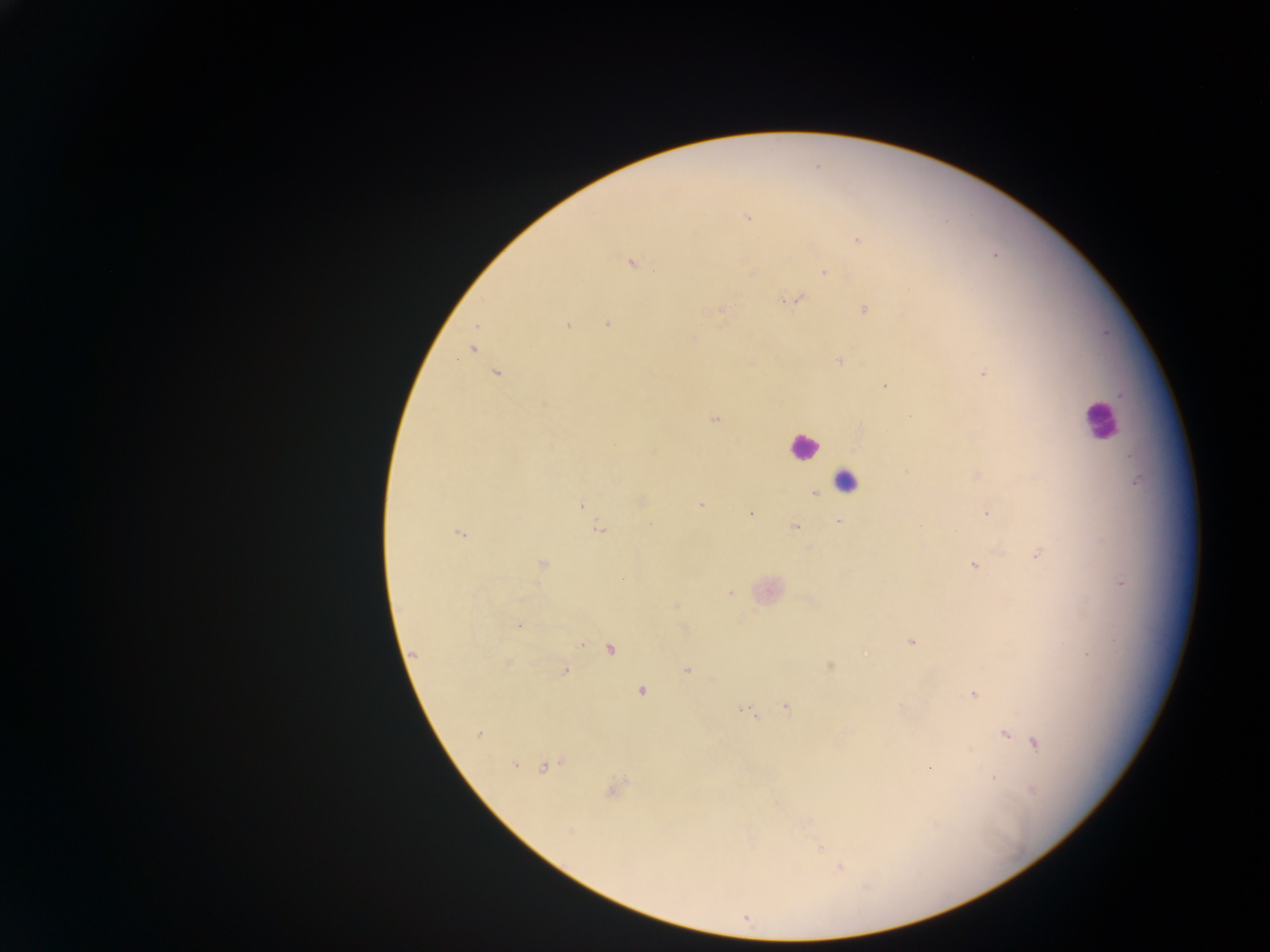

Approximate centers as (x, y) in pixels.
Summary:
  - Leukocyte locations: (1098, 419), (803, 446), (845, 482)
  - Plasmodium parasite locations: (747, 217), (857, 239), (630, 262), (825, 271), (795, 299), (864, 309), (719, 311), (607, 324), (477, 325), (567, 325), (692, 340), (472, 350), (840, 360), (496, 373), (984, 373), (885, 386), (714, 419), (907, 471), (978, 475), (814, 493), (641, 501), (580, 505), (700, 505), (986, 513), (750, 514), (838, 522), (795, 526), (599, 530), (459, 533), (1037, 555), (542, 563), (973, 565), (1122, 583), (731, 593), (677, 604), (519, 625), (911, 642), (581, 644), (610, 649), (413, 653), (830, 667), (687, 669), (565, 671), (641, 691), (973, 695), (786, 706), (746, 712), (478, 734), (1005, 734), (1036, 743), (514, 764), (547, 766), (929, 768), (994, 778), (613, 790), (1033, 791), (571, 830), (820, 848), (840, 868)
  - Preparation: thick blood film
  - Country: Ghana
  - Image size: 1270×952 pixels
  - Field of view: single
  - Capture: mobile-phone photograph through a microscope